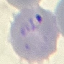

Malaria status: parasitized. Thin blood smear. Cell patch, automatically extracted from a larger field of view and resized to 64 × 64 pixels. Giemsa stain. Acquired by smartphone through the microscope eyepiece.